Assess the morphology of the red blood cells.
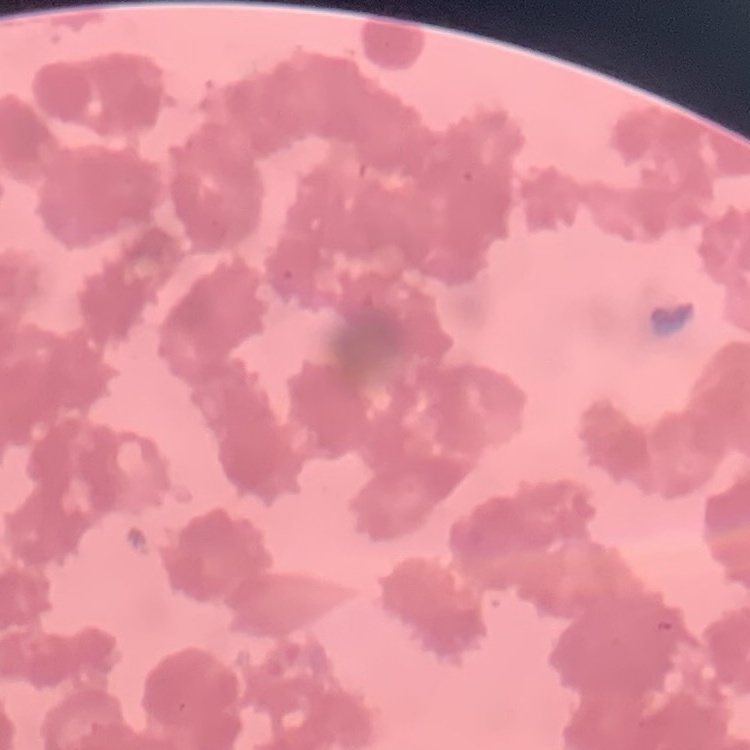

Rouleaux formation.

stain = Field's or Giemsa
image type = square crop of a larger photomicrograph
preparation = thin blood smear